Assess this cell for malaria.
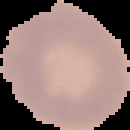

It is uninfected.

Image is 130×130 pixels. From a thin blood film. Cell region segmented out of the field of view; the surrounding area is masked to black.